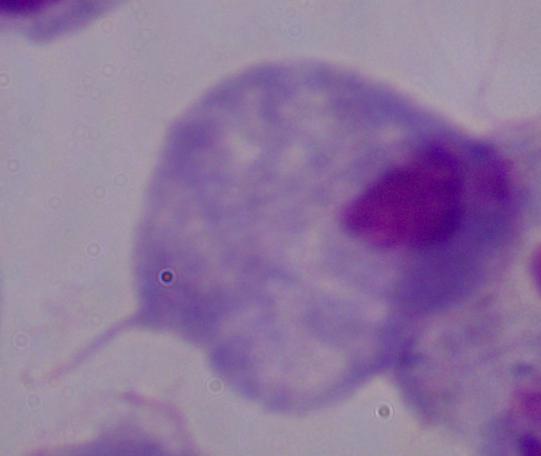
Micrograph. 1000x magnification. A trichomonad is shown.